Locate every leukocyte (white blood cell).
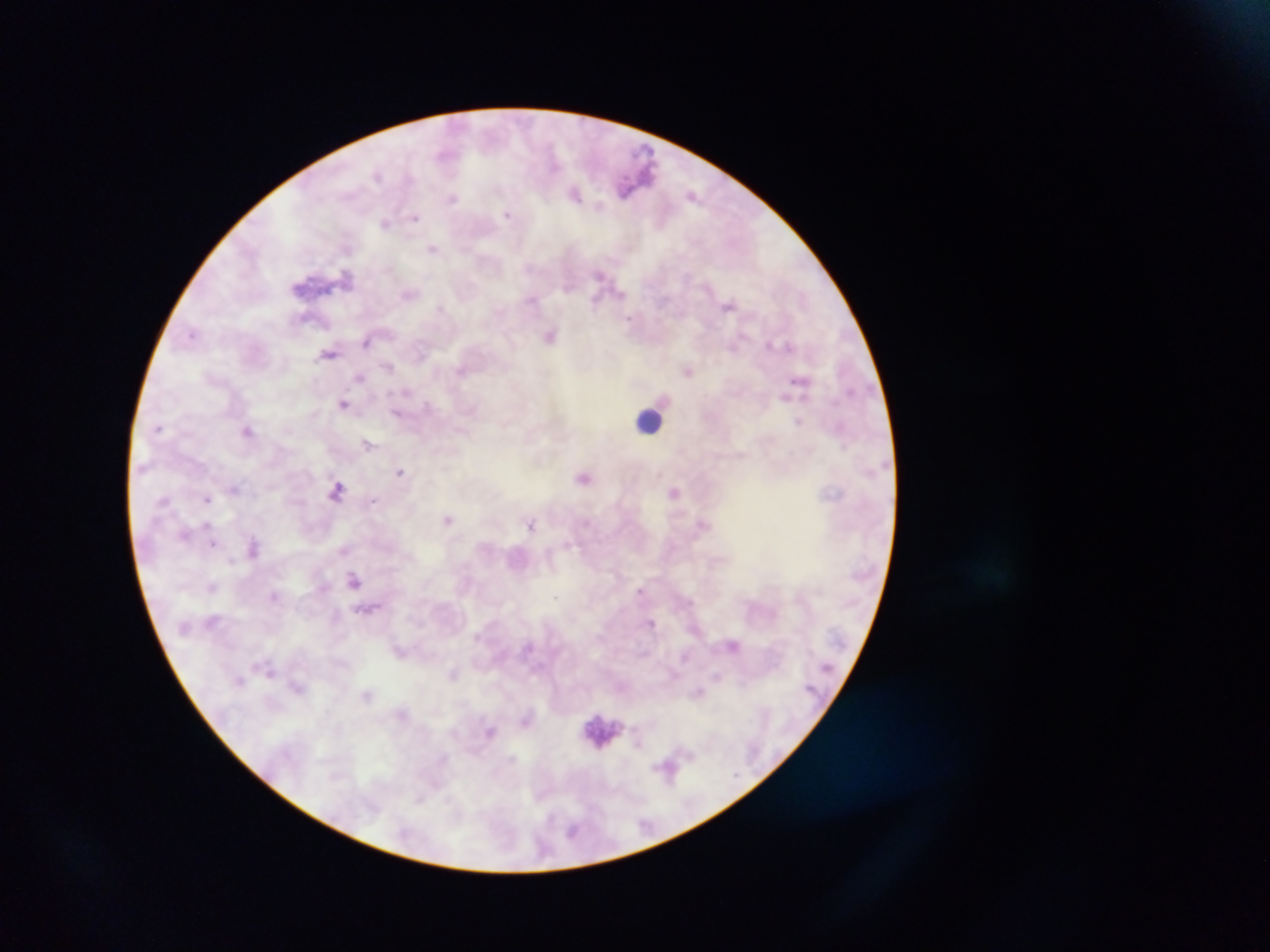

Approximate centers as {x, y} in pixels.
Leukocytes: {649, 421}, {605, 732}.

Plasmodium parasite locations: {377, 174}, {575, 194}, {692, 194}, {452, 198}, {599, 206}, {507, 214}, {415, 217}, {386, 223}, {433, 249}, {600, 274}, {348, 276}, {567, 287}, {408, 294}, {620, 294}, {532, 300}, {595, 302}, {729, 304}, {441, 307}, {629, 319}, {191, 335}, {550, 335}, {366, 342}, {770, 343}, {733, 345}, {789, 345}, {330, 353}, {388, 366}, {461, 370}, {689, 371}, {359, 377}, {798, 380}, {407, 391}, {785, 397}, {344, 403}, {427, 405}, {396, 414}, {798, 421}, {159, 427}, {248, 430}, {368, 444}, {400, 472}, {583, 478}, {234, 489}, {337, 491}, {675, 491}, {206, 498}, {164, 500}, {373, 500}, {448, 519}, {531, 523}, {208, 525}, {185, 534}, {214, 544}, {569, 544}, {254, 547}, {344, 550}, {231, 560}, {354, 580}, {212, 587}, {640, 590}, {272, 596}, {555, 596}, {690, 601}, {652, 623}, {732, 645}, {400, 651}, {685, 656}, {271, 672}, {453, 673}, {717, 676}, {742, 683}, {297, 688}, {698, 693}, {367, 695}, {490, 731}, {689, 754}, {666, 767}, {420, 799}, {572, 831}. Mobile-phone photograph taken through the microscope. Thick blood film. Single field of view. Sample from Ghana. Image is 1270×952 pixels.